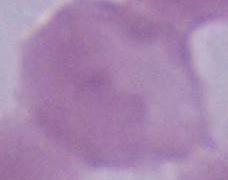

Captured at 1000x magnification. Photomicrograph. An erythrocyte is seen.